Report the malaria status of this cell.
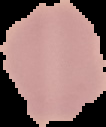

It is uninfected.

image size = 106×127 pixels
image type = cell region segmented out of the field of view; surrounding area masked to black
preparation = thin blood film